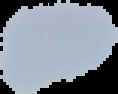
preparation = thin blood film
malaria status = uninfected
image size = 118×94 pixels
image type = segmented cell region on a black background